Name the parasite shown.
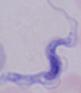
A trypanosome.

Summary:
  - Magnification: 1000x
  - Modality: micrograph